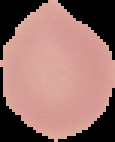

image_type: segmented cell region on a black background
result: no malaria parasites detected
preparation: thin blood smear
image_size: 115×142 pixels